Assess this cell for malaria.
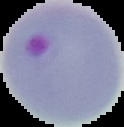
Parasitized.

Summary:
  - Image type: cell region segmented out of the field of view; surrounding area masked to black
  - Image size: 124×127 pixels
  - Preparation: thin blood film